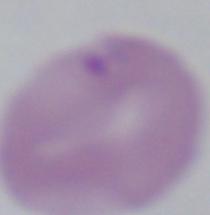

Summary:
  - Modality: micrograph
  - Magnification: 1000x
  - Identification: Babesia